Classify this cell by malaria status.
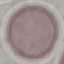
Uninfected.

Summary:
  - Preparation: thin blood smear
  - Capture: smartphone through the microscope eyepiece
  - Image type: cell patch, automatically extracted from a larger field of view and resized to 64 × 64 pixels
  - Stain: Giemsa